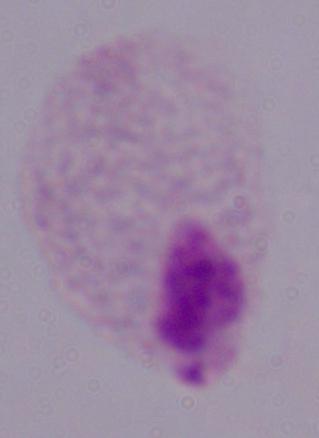
Summary:
  - Magnification: 1000x
  - Modality: micrograph
  - Identification: trichomonad